Outline each blood parasite and name the species.
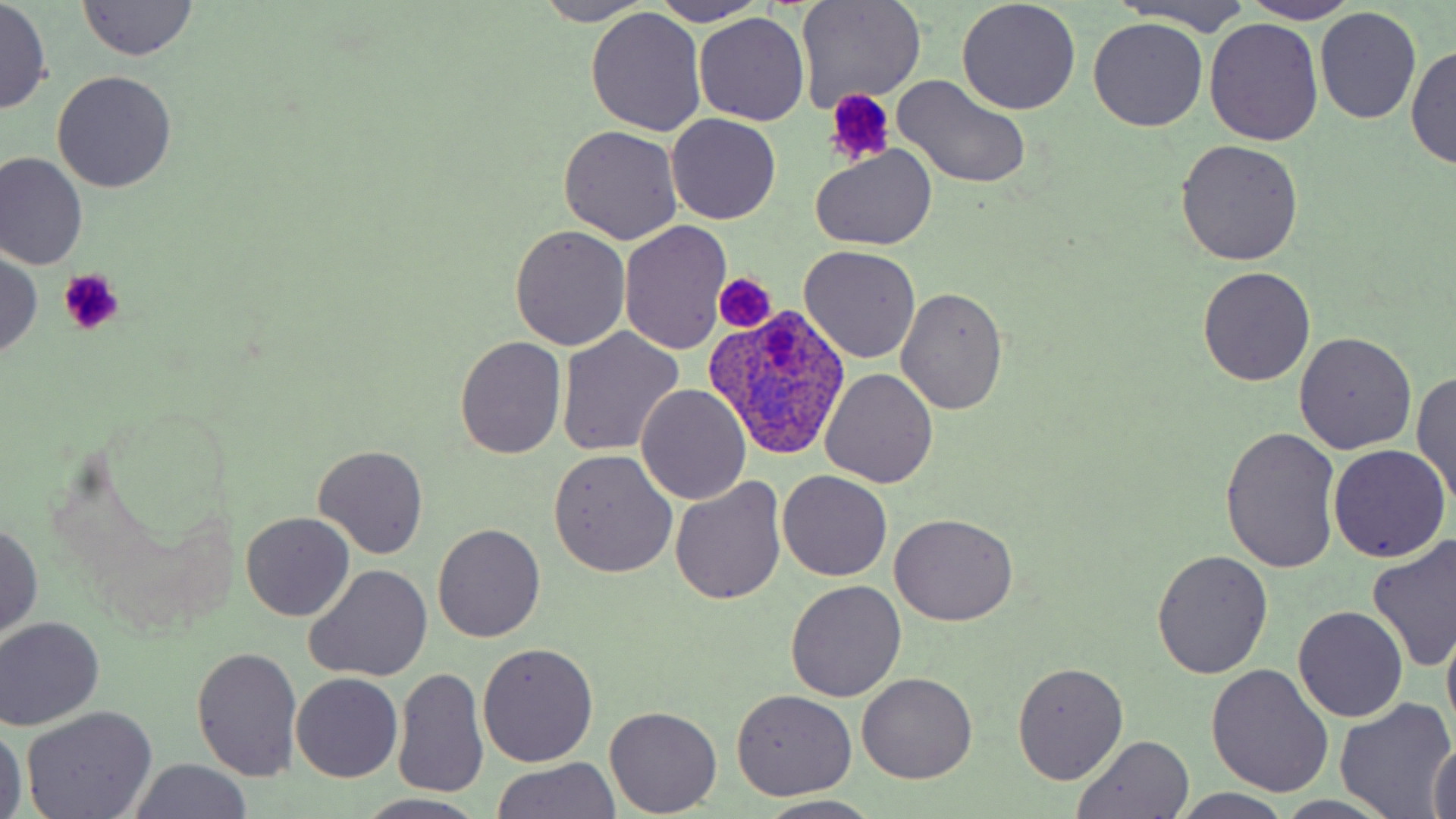
Approximate bounding boxes as [x1, y1, x2, y2] in pixels.
Plasmodium ovale-infected red blood cells: [706, 303, 851, 462].
No Plasmodium falciparum, Plasmodium malariae, Plasmodium vivax, Babesia divergens, or Trypanosoma brucei observed.

Summary:
  - Uninfected red blood cell locations: [795, 0, 927, 112], [1107, 0, 1258, 36], [1, 1, 51, 113], [76, 1, 199, 60], [650, 1, 768, 26], [1246, 1, 1360, 23], [532, 2, 657, 25], [956, 2, 1082, 115], [1314, 7, 1422, 124], [586, 9, 706, 136], [694, 13, 808, 126], [1088, 18, 1211, 132], [1204, 19, 1323, 147], [1408, 44, 1455, 170], [52, 70, 176, 192], [894, 75, 1032, 190], [667, 113, 781, 224], [558, 124, 683, 245], [1175, 139, 1305, 265], [811, 144, 935, 249], [1, 154, 88, 272], [621, 222, 731, 355], [509, 226, 631, 351], [799, 245, 921, 364], [0, 251, 44, 360], [1197, 267, 1316, 387], [895, 286, 1007, 413], [556, 328, 685, 455], [1293, 333, 1416, 455], [454, 336, 567, 458], [822, 368, 940, 488], [1412, 369, 1456, 508], [637, 383, 752, 505], [1221, 426, 1341, 574], [313, 445, 428, 560], [1329, 447, 1450, 563], [548, 449, 677, 578], [777, 470, 892, 581], [672, 478, 784, 604], [241, 512, 354, 621], [889, 512, 1020, 625], [0, 521, 44, 640], [433, 523, 544, 643], [1368, 535, 1456, 673], [1151, 551, 1273, 680], [305, 563, 433, 682], [786, 580, 907, 701], [1293, 606, 1408, 723], [0, 617, 104, 729], [1442, 618, 1456, 743], [4, 626, 132, 814], [478, 643, 598, 768], [193, 646, 303, 779], [1205, 662, 1334, 798], [1012, 663, 1129, 784], [394, 666, 489, 802], [857, 672, 978, 785], [293, 673, 402, 782], [731, 689, 857, 800], [1336, 698, 1454, 817], [606, 707, 720, 816], [22, 708, 156, 819], [0, 722, 26, 819], [1070, 735, 1196, 818], [1429, 737, 1456, 819], [487, 759, 623, 817], [126, 760, 256, 817], [1171, 790, 1298, 819], [360, 794, 486, 818], [753, 796, 885, 819]
  - Platelet locations: [825, 89, 895, 164], [59, 268, 126, 336], [714, 274, 774, 330]
  - Slide-level diagnosis: Plasmodium ovale
  - Magnification: 1000x
  - Modality: light microscopy
  - Field of view: single
  - Stain: May-Grünwald-Giemsa
  - Image size: 1456×819 pixels
  - Preparation: thin blood film